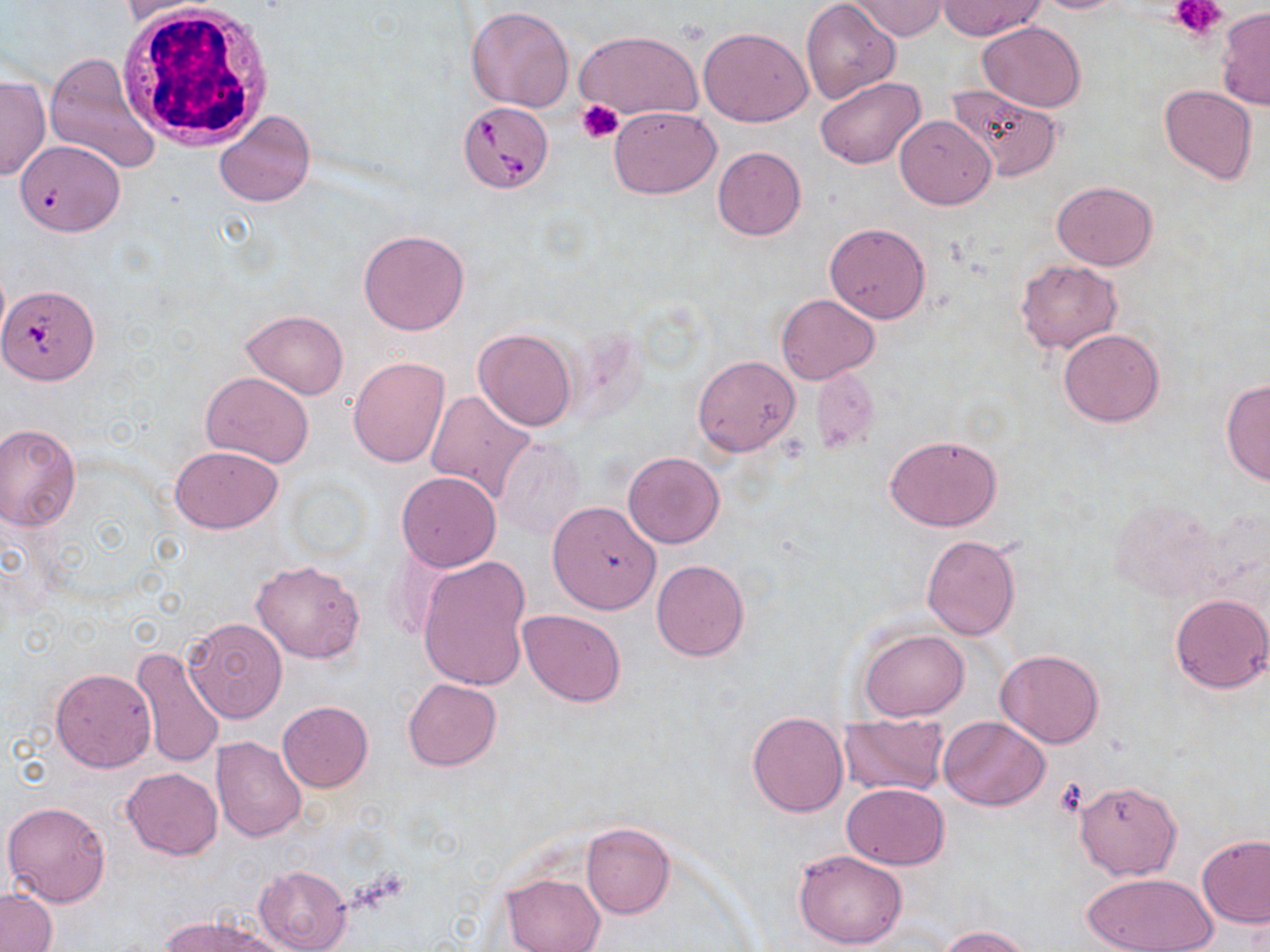
slide-level diagnosis = Babesia divergens
modality = optical microscopy
magnification = 1000x
stain = May-Grünwald-Giemsa
white blood cell locations = approximate bounding boxes as named x1/y1/x2/y2 corners in pixels: (x1=117, y1=5, x2=273, y2=152)
preparation = thin blood film
uninfected red blood cell locations = approximate bounding boxes as named x1/y1/x2/y2 corners in pixels: (x1=847, y1=0, x2=949, y2=40), (x1=1030, y1=0, x2=1128, y2=13), (x1=118, y1=1, x2=224, y2=24), (x1=802, y1=1, x2=901, y2=104), (x1=938, y1=1, x2=1046, y2=39), (x1=465, y1=6, x2=574, y2=112), (x1=1216, y1=7, x2=1270, y2=111), (x1=979, y1=21, x2=1084, y2=112), (x1=699, y1=26, x2=813, y2=126), (x1=574, y1=29, x2=703, y2=122), (x1=45, y1=51, x2=159, y2=174), (x1=0, y1=73, x2=49, y2=181), (x1=815, y1=77, x2=921, y2=170), (x1=946, y1=83, x2=1063, y2=180), (x1=1159, y1=85, x2=1258, y2=186), (x1=609, y1=106, x2=720, y2=199), (x1=214, y1=109, x2=316, y2=207), (x1=894, y1=114, x2=996, y2=210), (x1=14, y1=142, x2=131, y2=239), (x1=712, y1=146, x2=807, y2=241), (x1=1053, y1=181, x2=1157, y2=270), (x1=824, y1=222, x2=931, y2=323), (x1=357, y1=229, x2=470, y2=336), (x1=1014, y1=259, x2=1122, y2=353), (x1=777, y1=293, x2=880, y2=385), (x1=241, y1=309, x2=348, y2=399), (x1=1058, y1=328, x2=1166, y2=426), (x1=473, y1=329, x2=577, y2=431), (x1=693, y1=355, x2=800, y2=457), (x1=348, y1=356, x2=450, y2=467), (x1=809, y1=367, x2=879, y2=455), (x1=201, y1=371, x2=315, y2=469), (x1=1220, y1=380, x2=1270, y2=485), (x1=424, y1=388, x2=538, y2=503), (x1=0, y1=423, x2=81, y2=532), (x1=884, y1=433, x2=1003, y2=531), (x1=495, y1=435, x2=587, y2=544), (x1=170, y1=444, x2=283, y2=533), (x1=623, y1=451, x2=725, y2=548), (x1=396, y1=471, x2=501, y2=571), (x1=1109, y1=499, x2=1220, y2=603), (x1=547, y1=502, x2=661, y2=613), (x1=921, y1=535, x2=1021, y2=641), (x1=418, y1=557, x2=533, y2=693), (x1=251, y1=559, x2=367, y2=664), (x1=651, y1=559, x2=750, y2=662), (x1=1169, y1=593, x2=1269, y2=695), (x1=518, y1=610, x2=627, y2=707), (x1=183, y1=616, x2=288, y2=722), (x1=857, y1=627, x2=969, y2=720), (x1=132, y1=645, x2=224, y2=768), (x1=997, y1=648, x2=1104, y2=748), (x1=51, y1=667, x2=156, y2=772), (x1=403, y1=678, x2=501, y2=770), (x1=277, y1=701, x2=373, y2=792), (x1=748, y1=711, x2=848, y2=816), (x1=837, y1=713, x2=949, y2=797), (x1=938, y1=716, x2=1049, y2=811), (x1=211, y1=737, x2=307, y2=842), (x1=121, y1=767, x2=222, y2=860), (x1=1074, y1=779, x2=1182, y2=879), (x1=841, y1=783, x2=950, y2=869), (x1=3, y1=799, x2=111, y2=907), (x1=581, y1=822, x2=675, y2=919), (x1=1197, y1=834, x2=1270, y2=929), (x1=792, y1=849, x2=909, y2=950), (x1=253, y1=864, x2=351, y2=952), (x1=1081, y1=870, x2=1215, y2=952), (x1=502, y1=873, x2=604, y2=952), (x1=0, y1=889, x2=56, y2=951), (x1=159, y1=914, x2=288, y2=952), (x1=938, y1=925, x2=1035, y2=951)
image size = 1270×952 pixels
Babesia divergens-infected red blood cell locations = approximate bounding boxes as named x1/y1/x2/y2 corners in pixels: (x1=459, y1=100, x2=552, y2=192), (x1=1, y1=285, x2=98, y2=384)
field of view = single
platelet locations = approximate bounding boxes as named x1/y1/x2/y2 corners in pixels: (x1=1173, y1=0, x2=1227, y2=42), (x1=577, y1=101, x2=623, y2=144), (x1=1056, y1=778, x2=1087, y2=815)